Locate every malaria parasite and every leukocyte.
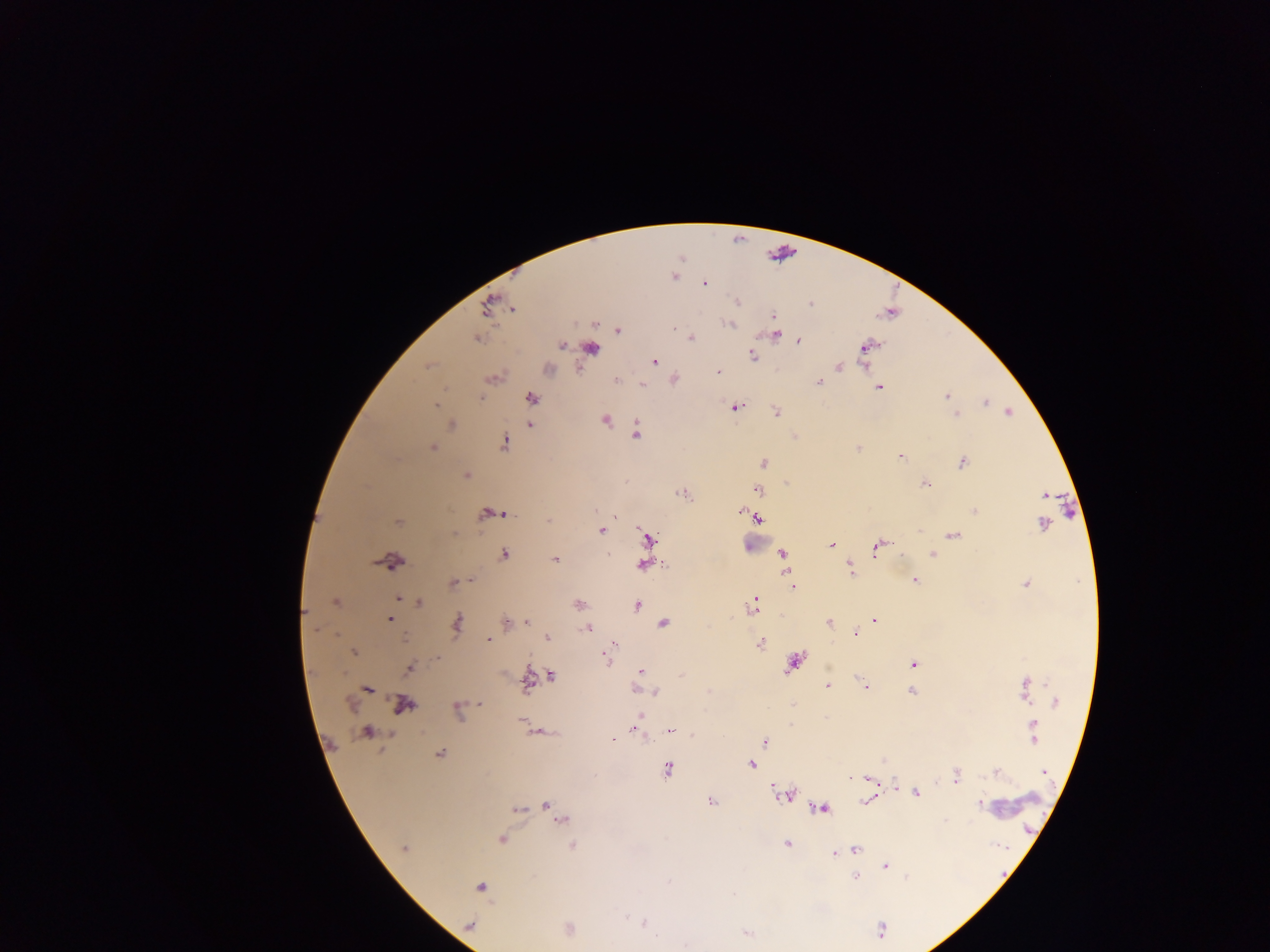
Approximate centers as {x, y} in pixels.
Malaria parasites: {674, 276}, {703, 282}, {736, 300}, {489, 304}, {812, 304}, {513, 308}, {772, 317}, {594, 323}, {730, 324}, {673, 328}, {617, 330}, {774, 335}, {476, 338}, {691, 338}, {797, 340}, {561, 345}, {591, 347}, {865, 347}, {753, 355}, {654, 361}, {865, 362}, {428, 365}, {838, 366}, {547, 369}, {717, 372}, {493, 377}, {616, 379}, {673, 379}, {819, 381}, {641, 385}, {879, 387}, {946, 396}, {481, 398}, {530, 398}, {984, 402}, {437, 404}, {734, 406}, {775, 412}, {1008, 412}, {956, 415}, {606, 419}, {451, 424}, {529, 424}, {636, 432}, {504, 442}, {432, 447}, {858, 447}, {899, 455}, {962, 461}, {763, 462}, {466, 475}, {925, 483}, {757, 490}, {683, 494}, {1044, 495}, {974, 510}, {741, 511}, {502, 513}, {490, 514}, {614, 515}, {754, 517}, {757, 518}, {548, 519}, {397, 522}, {1042, 524}, {601, 530}, {952, 534}, {647, 540}, {831, 545}, {879, 545}, {782, 553}, {932, 553}, {504, 554}, {390, 559}, {555, 559}, {643, 565}, {849, 568}, {471, 580}, {914, 580}, {453, 582}, {1026, 584}, {793, 585}, {399, 599}, {755, 599}, {412, 600}, {336, 601}, {419, 602}, {577, 604}, {636, 605}, {753, 605}, {390, 617}, {874, 620}, {829, 622}, {505, 623}, {527, 623}, {456, 624}, {663, 624}, {587, 628}, {854, 633}, {547, 638}, {487, 639}, {759, 643}, {614, 644}, {353, 652}, {609, 653}, {605, 657}, {794, 663}, {913, 664}, {410, 668}, {640, 671}, {551, 676}, {527, 680}, {828, 686}, {866, 687}, {1025, 687}, {366, 688}, {636, 689}, {912, 690}, {655, 692}, {1054, 702}, {480, 703}, {403, 704}, {791, 705}, {457, 709}, {640, 715}, {523, 719}, {634, 726}, {671, 731}, {367, 732}, {539, 732}, {1033, 734}, {763, 741}, {439, 753}, {750, 764}, {667, 770}, {996, 772}, {1043, 772}, {955, 775}, {867, 778}, {894, 788}, {916, 793}, {787, 795}, {868, 800}, {710, 801}, {979, 804}, {545, 805}, {821, 808}, {517, 810}, {555, 813}, {562, 820}, {945, 820}, {501, 839}, {787, 843}, {572, 844}, {404, 848}, {855, 848}, {849, 850}, {835, 852}, {884, 866}, {855, 877}, {907, 877}, {480, 887}, {644, 923}, {469, 925}, {567, 930}, {746, 933}.
No leukocytes observed.

Summary:
  - Capture: mobile-phone photograph through a microscope
  - Image size: 1270×952 pixels
  - Country: Ghana
  - Preparation: thick blood film
  - Field of view: single